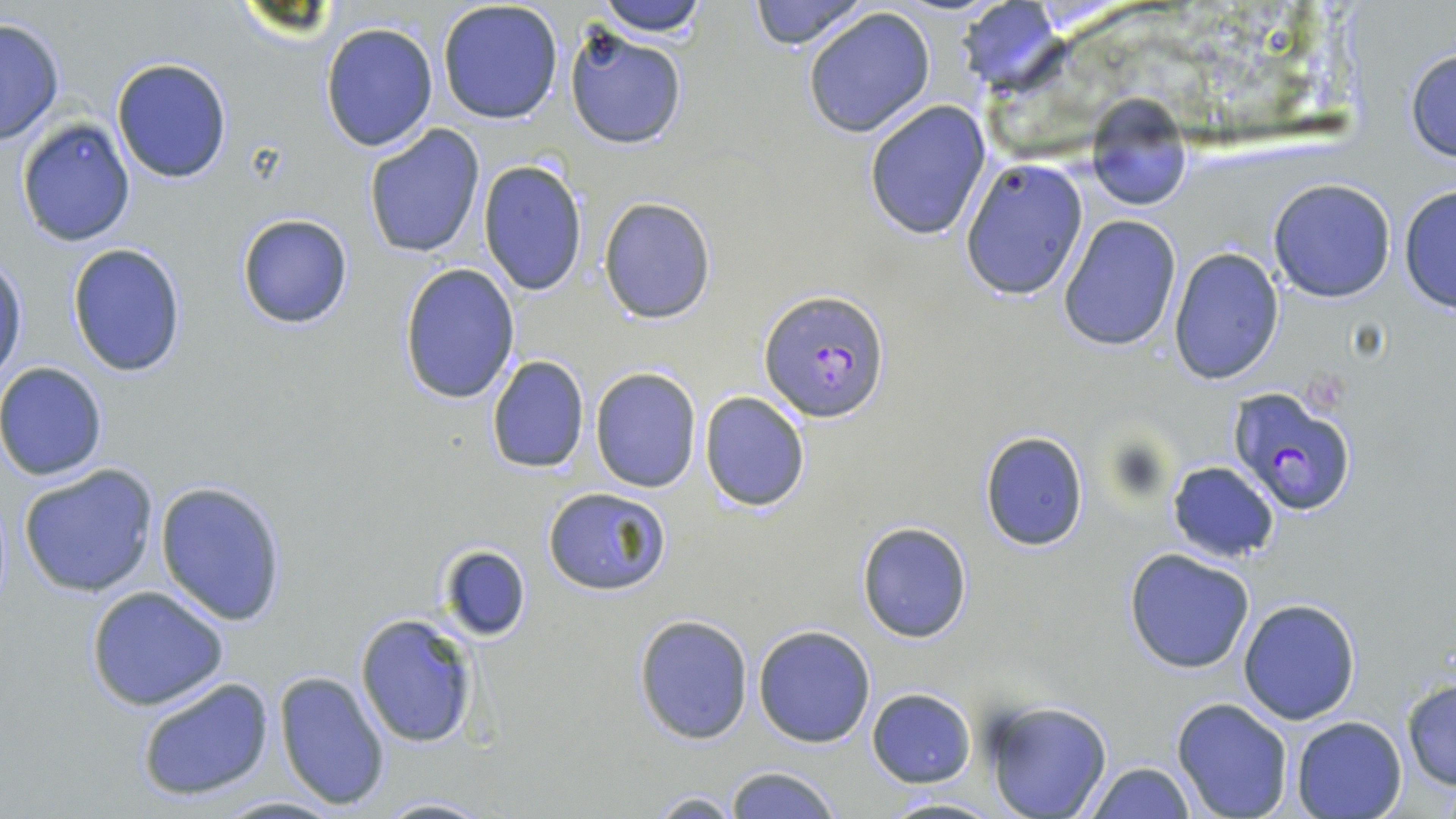
slide-level diagnosis = Plasmodium falciparum
magnification = 1000x
modality = optical microscopy
uninfected red blood cell locations = approximate bounding boxes as (x1,y1)-(x2,y2) corner pairs in pixels: (594,0)-(710,38), (748,0)-(870,51), (437,1)-(564,123), (953,1)-(1064,97), (802,7)-(935,139), (0,16)-(66,142), (321,21)-(438,151), (563,25)-(689,151), (1404,47)-(1456,163), (112,56)-(234,184), (1084,97)-(1194,213), (864,101)-(991,240), (16,116)-(137,247), (363,124)-(486,259), (959,157)-(1089,300), (477,158)-(588,296), (1267,178)-(1397,303), (1398,185)-(1455,313), (597,197)-(716,325), (236,211)-(356,330), (1058,214)-(1182,351), (67,242)-(189,378), (1168,248)-(1286,384), (0,255)-(28,387), (399,263)-(521,404), (486,354)-(590,475), (0,361)-(111,481), (590,366)-(702,493), (699,390)-(811,513), (980,429)-(1090,552), (1167,461)-(1281,564), (16,463)-(160,598), (154,481)-(287,626), (543,486)-(672,596), (856,521)-(973,642), (438,544)-(532,643), (1124,549)-(1256,675), (86,586)-(229,713), (1239,599)-(1360,724), (355,612)-(480,749), (633,614)-(755,745), (752,625)-(877,747), (274,670)-(392,811), (134,674)-(276,804), (1400,679)-(1456,792), (866,688)-(976,787), (1171,698)-(1294,819), (981,700)-(1112,818), (1290,716)-(1407,819), (1081,761)-(1199,818), (723,766)-(840,819), (647,791)-(742,817), (362,794)-(499,818), (876,794)-(1004,818), (211,795)-(346,818)
field of view = one of a larger specimen
preparation = thin blood film
Plasmodium falciparum-infected red blood cell locations = approximate bounding boxes as (x1,y1)-(x2,y2) corner pairs in pixels: (761,288)-(889,424), (1229,385)-(1360,516)
stain = May-Grünwald-Giemsa
image size = 1456×819 pixels